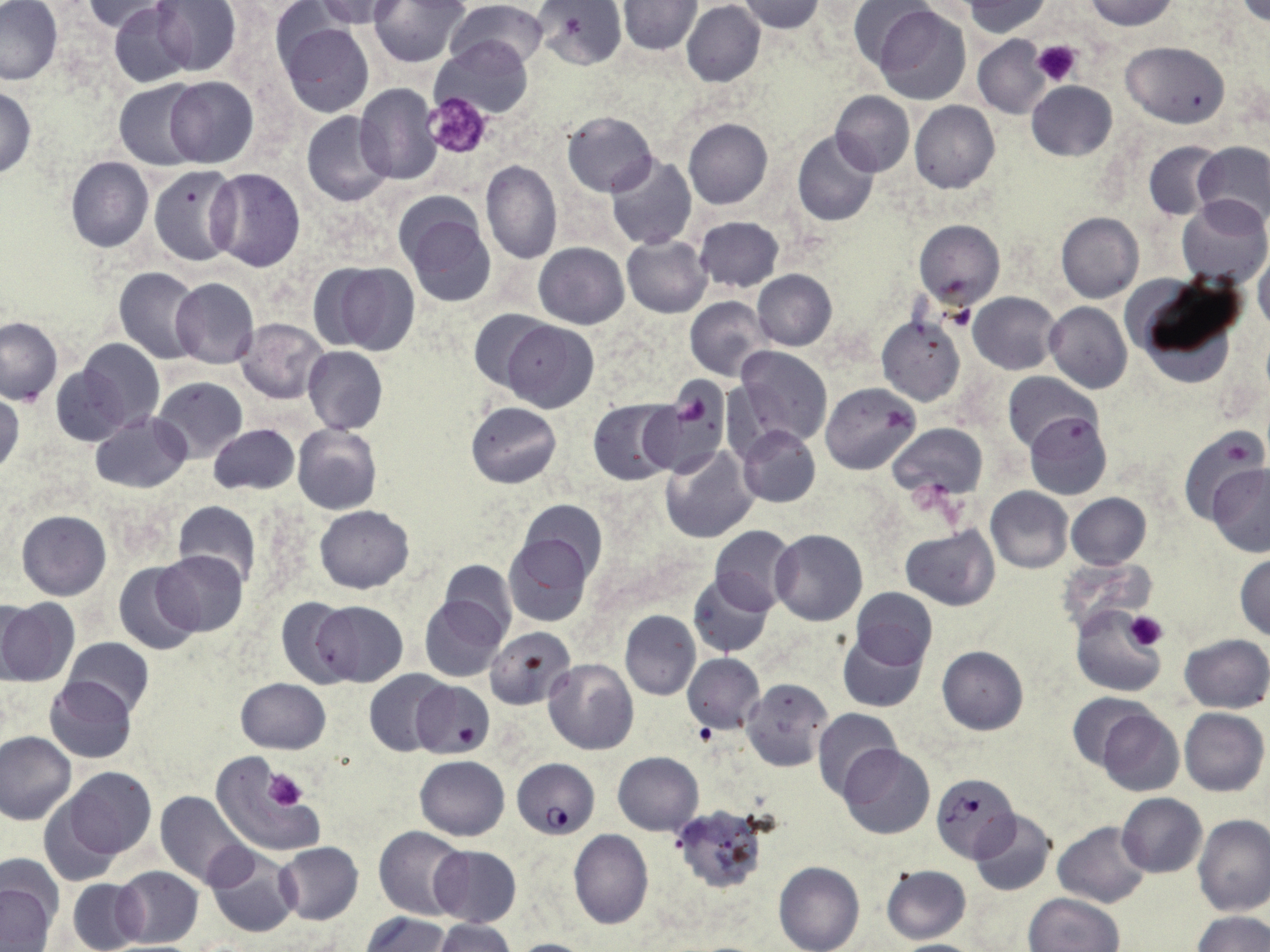

Summary:
  - Coordinate format: approximate bounding boxes as (x1,y1)-(x2,y2) corner pairs in pixels
  - Plasmodium falciparum-infected red blood cell locations: (511,757)-(600,838), (931,773)-(1018,861)
  - Platelet locations: (1030,40)-(1082,86), (422,91)-(492,159), (676,391)-(709,428), (1124,611)-(1167,652), (263,770)-(308,810)
  - Uninfected red blood cell locations: (0,0)-(64,86), (79,0)-(177,33), (150,0)-(241,75), (310,0)-(408,29), (370,0)-(470,67), (448,0)-(550,70), (534,0)-(626,70), (736,0)-(825,33), (961,0)-(1052,37), (1083,0)-(1179,31), (619,1)-(701,54), (847,1)-(938,79), (1235,1)-(1269,26), (681,2)-(765,87), (108,3)-(196,87), (874,5)-(969,102), (276,16)-(375,118), (433,36)-(533,119), (972,36)-(1051,118), (1122,41)-(1231,127), (164,77)-(258,168), (113,80)-(201,169), (1025,81)-(1117,161), (355,84)-(444,184), (0,86)-(36,178), (831,91)-(914,175), (911,101)-(999,193), (561,110)-(658,196), (301,111)-(395,206), (682,117)-(772,209), (793,130)-(880,227), (1144,141)-(1226,221), (1193,141)-(1270,229), (605,156)-(697,251), (65,157)-(154,252), (479,159)-(561,263), (148,165)-(240,266), (207,167)-(306,271), (397,194)-(497,307), (1176,196)-(1269,286), (1056,212)-(1144,303), (692,216)-(785,293), (914,220)-(1005,308), (621,235)-(712,317), (534,243)-(629,329), (1254,255)-(1270,331), (314,261)-(420,354), (115,267)-(204,363), (753,270)-(837,350), (1130,276)-(1246,387), (170,278)-(259,368), (969,292)-(1060,374), (686,296)-(771,380), (1044,301)-(1132,393), (469,310)-(556,393), (877,315)-(968,407), (1,316)-(62,405), (236,318)-(327,404), (501,320)-(598,412), (74,339)-(165,437), (303,346)-(387,435), (735,346)-(833,446), (50,358)-(135,446), (1003,373)-(1097,451), (153,376)-(248,462), (641,383)-(728,476), (821,383)-(920,474), (0,390)-(23,478), (588,399)-(679,485), (466,402)-(561,488), (1024,411)-(1112,501), (90,412)-(191,492), (209,423)-(298,495), (890,423)-(987,501), (293,424)-(382,515), (738,426)-(820,507), (1180,428)-(1265,526), (660,445)-(758,543), (1207,464)-(1270,558), (985,487)-(1072,572), (1065,493)-(1151,570), (171,500)-(262,589), (519,500)-(608,582), (315,505)-(414,593), (16,510)-(111,599), (709,525)-(798,613), (900,527)-(999,610), (771,529)-(868,625), (503,533)-(592,627), (155,550)-(248,635), (1235,554)-(1270,640), (439,560)-(516,640), (114,561)-(202,657), (687,573)-(774,658), (851,589)-(937,669), (419,596)-(510,683), (276,597)-(358,688), (0,598)-(76,686), (312,601)-(408,686), (1071,604)-(1165,698), (620,610)-(700,699), (485,627)-(577,711), (838,631)-(927,712), (1179,634)-(1270,712), (63,637)-(154,717), (937,647)-(1028,734), (683,653)-(765,734), (544,658)-(639,754), (365,669)-(452,756), (43,677)-(137,763), (742,678)-(831,771), (236,679)-(330,753), (410,680)-(495,758), (1068,693)-(1155,768), (812,707)-(903,801), (1179,707)-(1268,796), (1095,708)-(1184,796), (0,730)-(76,826), (837,743)-(935,840), (613,752)-(703,834), (415,755)-(509,839), (212,759)-(318,854), (63,767)-(155,858), (155,791)-(251,888), (1117,793)-(1207,877), (38,798)-(123,887), (670,807)-(768,896), (968,809)-(1057,898), (1193,815)-(1269,915), (1052,820)-(1151,908), (375,826)-(467,919), (569,829)-(654,931), (275,842)-(363,924), (429,845)-(521,927), (205,850)-(298,938), (774,861)-(864,952), (880,863)-(971,944), (111,866)-(203,948), (69,878)-(145,951), (0,881)-(57,952), (1025,893)-(1124,952), (362,912)-(451,952), (1194,912)-(1270,952), (433,919)-(516,952), (507,938)-(597,951), (884,939)-(988,952)
  - Slide-level diagnosis: Plasmodium falciparum
  - Magnification: 1000x
  - Preparation: thin blood film
  - Field of view: single
  - Stain: May-Grünwald-Giemsa
  - Image size: 1270×952 pixels
  - Modality: light microscopy